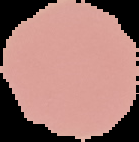
Summary:
  - Result: no Plasmodium parasites seen
  - Image size: 139×142 pixels
  - Image type: segmented cell region on a black background
  - Preparation: thin blood film